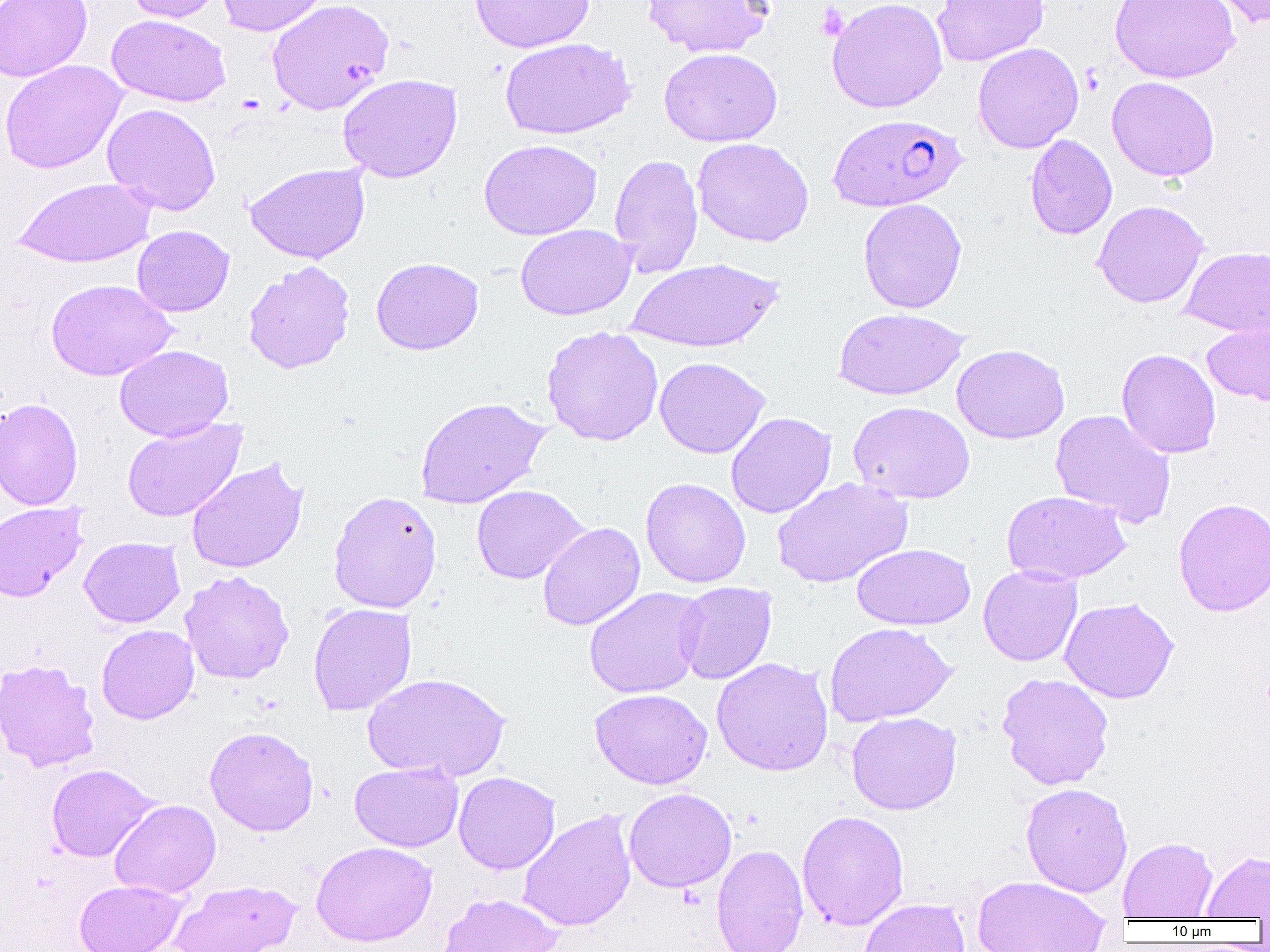
slide-level diagnosis = Plasmodium falciparum
platelet locations = approximate bounding boxes as [x1, y1, x2, y2] in pixels: [816, 3, 849, 42]
modality = optical microscopy
image size = 1270×952 pixels
uninfected red blood cell locations = approximate bounding boxes as [x1, y1, x2, y2] in pixels: [0, 0, 93, 82], [124, 0, 227, 23], [216, 0, 329, 36], [266, 0, 395, 115], [470, 0, 595, 53], [643, 0, 775, 58], [826, 0, 947, 113], [932, 0, 1049, 66], [1109, 0, 1240, 83], [1206, 0, 1270, 28], [107, 15, 231, 106], [499, 37, 636, 140], [972, 42, 1084, 153], [659, 47, 782, 147], [0, 59, 128, 174], [338, 74, 462, 183], [1106, 76, 1220, 181], [102, 103, 221, 215], [1025, 134, 1117, 240], [692, 137, 813, 247], [479, 139, 602, 240], [609, 153, 703, 278], [245, 163, 370, 264], [12, 177, 156, 268], [858, 198, 967, 313], [1092, 200, 1209, 308], [515, 224, 636, 320], [132, 225, 234, 316], [1180, 246, 1270, 337], [371, 256, 484, 355], [625, 257, 783, 353], [243, 261, 355, 374], [46, 279, 177, 381], [834, 308, 967, 400], [1203, 320, 1270, 407], [541, 326, 663, 446], [951, 344, 1070, 444], [114, 345, 233, 442], [1116, 348, 1221, 459], [654, 357, 770, 458], [413, 396, 550, 509], [0, 398, 84, 510], [848, 401, 975, 504], [1050, 408, 1176, 528], [726, 412, 837, 519], [122, 418, 247, 522], [186, 458, 308, 573], [772, 477, 913, 588], [640, 478, 751, 588], [471, 484, 588, 585], [328, 490, 442, 613], [1001, 490, 1131, 584], [1173, 498, 1270, 617], [0, 501, 89, 602], [537, 521, 645, 631], [79, 536, 185, 627], [852, 543, 975, 630], [978, 565, 1082, 666], [179, 570, 294, 684], [675, 582, 777, 685], [583, 587, 708, 698], [1059, 597, 1179, 704], [308, 603, 417, 716], [824, 622, 956, 727], [96, 624, 199, 724], [711, 657, 834, 777], [0, 659, 100, 773], [996, 672, 1114, 790], [362, 673, 511, 782], [590, 688, 712, 789], [846, 711, 961, 815], [204, 726, 319, 836], [350, 762, 464, 852], [45, 763, 159, 862], [453, 772, 560, 874], [1020, 782, 1133, 897], [624, 787, 737, 892], [109, 799, 220, 899], [518, 809, 637, 932], [796, 810, 910, 930], [1118, 836, 1218, 920], [311, 841, 437, 947], [711, 843, 808, 952], [1201, 851, 1270, 919], [972, 875, 1110, 952], [74, 879, 186, 952], [170, 879, 300, 952], [438, 893, 564, 952], [859, 898, 970, 952]
magnification = 1000x
preparation = thin blood smear
field of view = single
Plasmodium falciparum-infected red blood cell locations = approximate bounding boxes as [x1, y1, x2, y2] in pixels: [828, 114, 967, 212]